Report the malaria status of this cell.
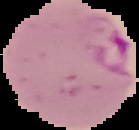

It is parasitized.

preparation = thin blood smear
image size = 139×130 pixels
image type = segmented cell region on a black background